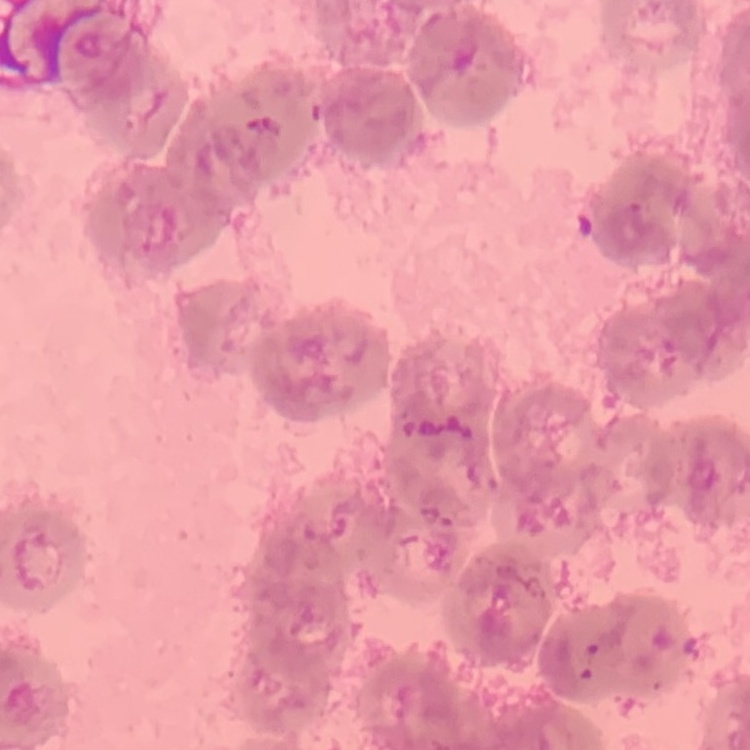

{
  "erythrocyte_morphology": "rouleaux formation",
  "image_type": "square crop of a larger photomicrograph",
  "preparation": "thin blood film",
  "stain": "Field's or Giemsa"
}